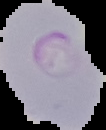
Summary:
  - Image size: 106×130 pixels
  - Malaria status: parasitized
  - Image type: segmented cell region with the area outside set to black
  - Preparation: thin blood film